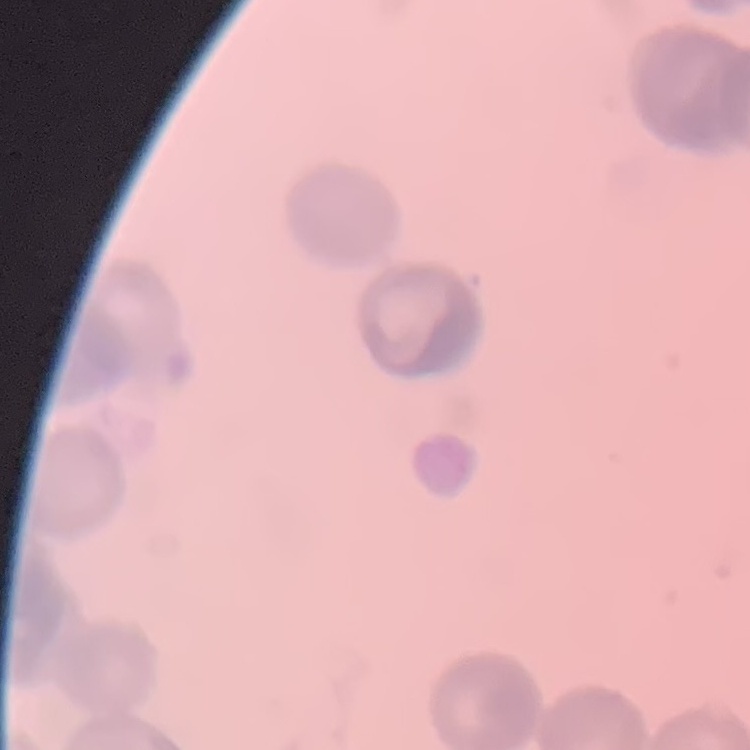

{
  "erythrocyte_morphology": "rouleaux formation",
  "image_type": "square crop of a larger photomicrograph",
  "stain": "Field's or Giemsa",
  "preparation": "thin blood smear"
}